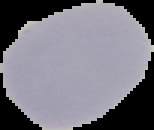

Summary:
  - Preparation: thin blood film
  - Image type: segmented cell region on a black background
  - Malaria status: uninfected
  - Image size: 154×130 pixels